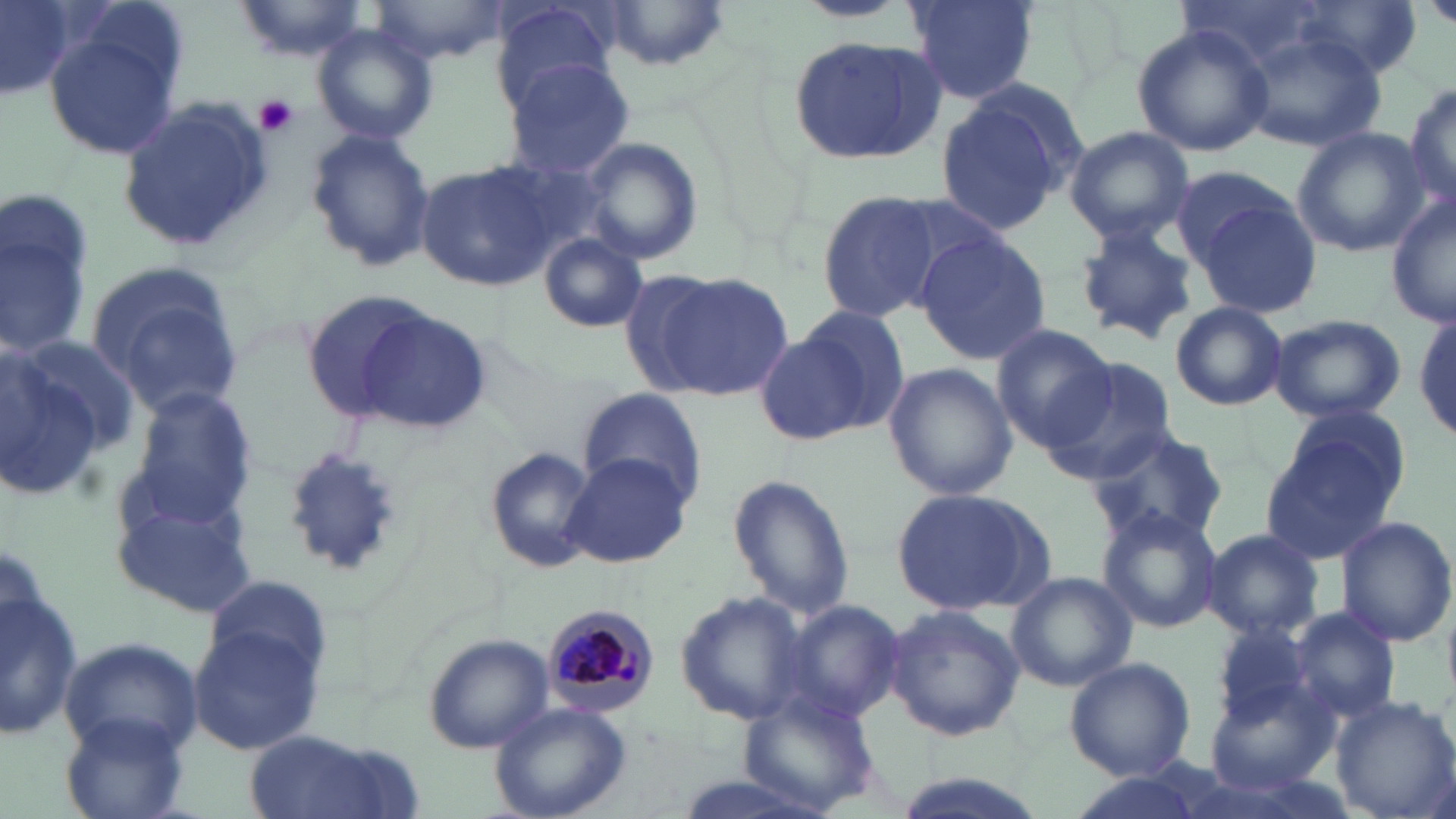

Summary:
  - Coordinate format: approximate bounding boxes as named x1/y1/x2/y2 corners in pixels
  - White blood cell locations: (x1=1, y1=531, x2=81, y2=764)
  - Platelet locations: (x1=254, y1=94, x2=300, y2=137)
  - Uninfected red blood cell locations: (x1=0, y1=0, x2=81, y2=100), (x1=229, y1=0, x2=371, y2=62), (x1=372, y1=0, x2=510, y2=64), (x1=794, y1=0, x2=909, y2=21), (x1=907, y1=0, x2=1038, y2=103), (x1=1423, y1=0, x2=1456, y2=33), (x1=600, y1=1, x2=729, y2=74), (x1=1300, y1=2, x2=1418, y2=80), (x1=493, y1=3, x2=615, y2=106), (x1=310, y1=23, x2=438, y2=148), (x1=40, y1=24, x2=184, y2=159), (x1=1133, y1=24, x2=1273, y2=157), (x1=1240, y1=32, x2=1385, y2=151), (x1=787, y1=36, x2=948, y2=166), (x1=505, y1=59, x2=632, y2=179), (x1=934, y1=79, x2=1086, y2=234), (x1=1404, y1=82, x2=1456, y2=214), (x1=117, y1=98, x2=272, y2=254), (x1=1063, y1=125, x2=1195, y2=245), (x1=303, y1=127, x2=436, y2=274), (x1=1292, y1=127, x2=1430, y2=257), (x1=578, y1=140, x2=704, y2=265), (x1=415, y1=161, x2=557, y2=291), (x1=1167, y1=165, x2=1300, y2=269), (x1=1191, y1=191, x2=1321, y2=321), (x1=821, y1=192, x2=944, y2=322), (x1=1388, y1=197, x2=1456, y2=328), (x1=2, y1=199, x2=96, y2=361), (x1=1073, y1=223, x2=1202, y2=345), (x1=913, y1=230, x2=1051, y2=368), (x1=538, y1=233, x2=648, y2=332), (x1=85, y1=264, x2=245, y2=417), (x1=642, y1=270, x2=793, y2=398), (x1=303, y1=288, x2=441, y2=424), (x1=1170, y1=302, x2=1287, y2=410), (x1=795, y1=304, x2=911, y2=431), (x1=345, y1=306, x2=495, y2=435), (x1=1415, y1=312, x2=1456, y2=443), (x1=1269, y1=313, x2=1407, y2=422), (x1=989, y1=324, x2=1119, y2=451), (x1=756, y1=332, x2=871, y2=444), (x1=0, y1=336, x2=116, y2=501), (x1=1042, y1=360, x2=1178, y2=485), (x1=883, y1=362, x2=1017, y2=502), (x1=123, y1=383, x2=258, y2=528), (x1=579, y1=389, x2=705, y2=506), (x1=1276, y1=407, x2=1411, y2=513), (x1=1084, y1=425, x2=1229, y2=550), (x1=1260, y1=431, x2=1403, y2=566), (x1=280, y1=445, x2=408, y2=582), (x1=482, y1=445, x2=601, y2=573), (x1=561, y1=454, x2=696, y2=572), (x1=727, y1=475, x2=854, y2=621), (x1=110, y1=483, x2=260, y2=621), (x1=890, y1=484, x2=1058, y2=618), (x1=1096, y1=507, x2=1223, y2=634), (x1=1336, y1=516, x2=1455, y2=647), (x1=1203, y1=529, x2=1321, y2=639), (x1=1007, y1=571, x2=1136, y2=691), (x1=206, y1=576, x2=331, y2=680), (x1=2, y1=583, x2=83, y2=740), (x1=674, y1=591, x2=813, y2=728), (x1=780, y1=597, x2=905, y2=725), (x1=884, y1=605, x2=1025, y2=741), (x1=1281, y1=606, x2=1401, y2=726), (x1=1210, y1=621, x2=1318, y2=728), (x1=187, y1=622, x2=327, y2=755), (x1=421, y1=633, x2=552, y2=754), (x1=61, y1=639, x2=199, y2=754), (x1=1065, y1=656, x2=1197, y2=782), (x1=1203, y1=674, x2=1340, y2=792), (x1=736, y1=689, x2=881, y2=815), (x1=1328, y1=695, x2=1456, y2=819), (x1=489, y1=701, x2=632, y2=819), (x1=62, y1=713, x2=190, y2=818), (x1=240, y1=731, x2=421, y2=819)
  - Plasmodium malariae-infected red blood cell locations: (x1=540, y1=600, x2=661, y2=715)
  - Slide-level diagnosis: Plasmodium malariae
  - Stain: May-Grünwald-Giemsa
  - Preparation: thin blood smear
  - Modality: light microscopy
  - Field of view: one of a larger specimen
  - Image size: 1456×819 pixels
  - Magnification: 1000x